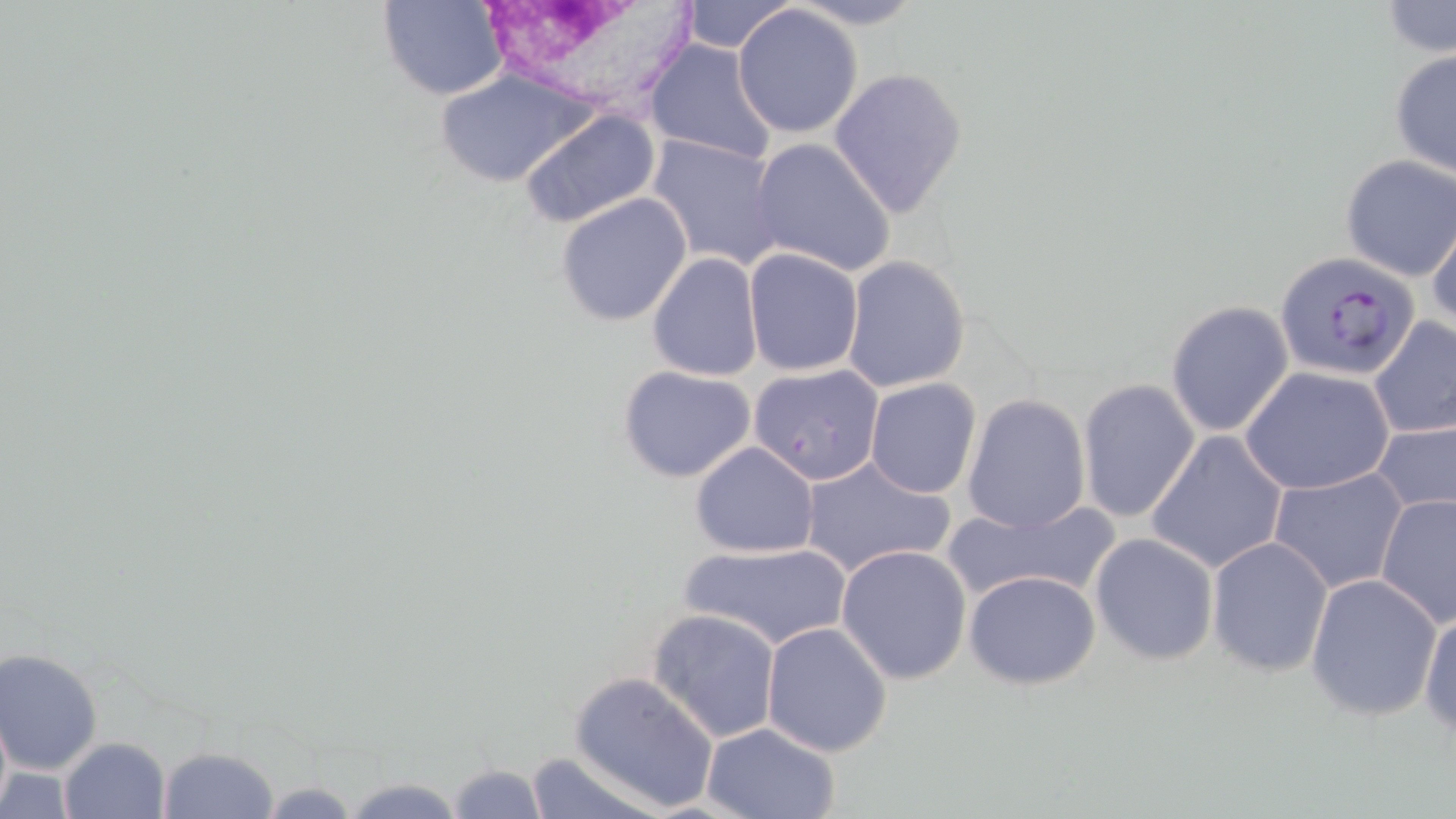
Approximate bounding boxes as (x1, y1, x2, y2) in pixels. Plasmodium falciparum-infected red blood cell locations: (1274, 251, 1419, 381). Uninfected red blood cell locations: (378, 0, 509, 100), (678, 0, 796, 53), (786, 0, 927, 30), (1380, 1, 1456, 58), (732, 4, 864, 139), (643, 39, 779, 166), (1389, 49, 1456, 180), (827, 67, 969, 219), (435, 69, 596, 188), (518, 107, 662, 229), (647, 133, 784, 272), (751, 138, 896, 278), (1339, 154, 1455, 281), (554, 190, 694, 326), (1426, 213, 1456, 335), (743, 246, 865, 376), (646, 252, 764, 380), (840, 255, 971, 394), (1165, 299, 1296, 438), (1368, 318, 1456, 440), (748, 363, 886, 486), (617, 365, 759, 484), (1241, 366, 1393, 494), (864, 379, 982, 498), (1076, 379, 1200, 523), (960, 394, 1091, 533), (1374, 417, 1456, 520), (1146, 430, 1289, 575), (689, 440, 821, 556), (799, 453, 956, 579), (1270, 467, 1405, 593), (1375, 490, 1455, 628), (941, 496, 1121, 605), (1089, 532, 1219, 666), (1206, 536, 1334, 678), (683, 541, 850, 648), (836, 545, 972, 685), (963, 569, 1101, 690), (1304, 573, 1443, 720), (1419, 603, 1456, 739), (647, 609, 782, 742), (762, 622, 894, 757), (0, 647, 104, 774), (568, 670, 720, 812), (701, 721, 843, 819), (59, 737, 173, 819), (156, 747, 280, 819), (525, 749, 661, 818), (445, 761, 546, 818), (337, 774, 473, 819), (254, 780, 366, 816). White blood cell locations: (488, 0, 700, 111). Slide-level diagnosis: Plasmodium falciparum. May-Grünwald-Giemsa-stained preparation. Light microscopy. Single field of view. Image is 1456×819 pixels. 1000x magnification. Thin blood smear.